Comment on the morphology of the red blood cells.
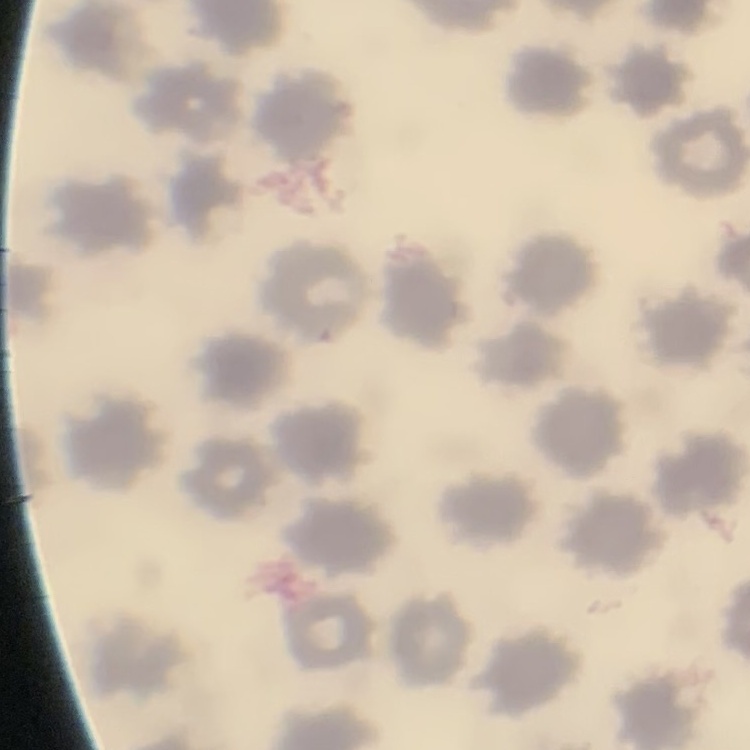

No rouleaux formation.

Summary:
  - Stain: Field's or Giemsa
  - Image type: one tile cut from a larger photomicrograph
  - Preparation: thin blood film